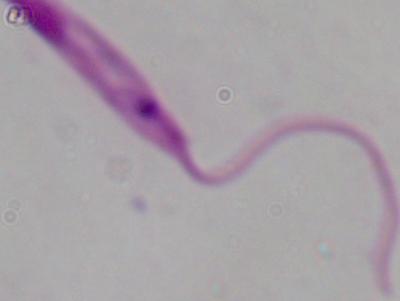

Summary:
  - Magnification: 1000x
  - Modality: photomicrograph
  - Identification: Leishmania